Assess this cell for malaria.
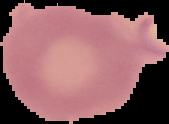

Uninfected.

{
  "preparation": "thin blood smear",
  "image_type": "cell region segmented out of the field of view; surrounding area masked to black",
  "image_size": "169×124 pixels"
}